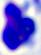
Captured at 400x magnification. A leukocyte is seen. Photomicrograph.